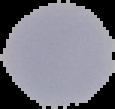
Summary:
  - Malaria status: uninfected
  - Image size: 115×109 pixels
  - Preparation: thin blood film
  - Image type: cell region segmented out of the field of view; surrounding area masked to black